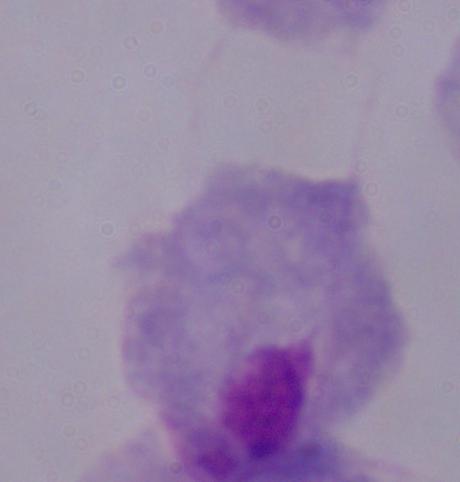

Photomicrograph. A trichomonad is seen. Captured at 1000x magnification.